Assess this cell for malaria.
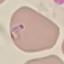
Parasitized.

stain: Giemsa
preparation: thin blood film
capture: smartphone camera at the microscope eyepiece
image_type: cell patch, automatically extracted from a larger field of view and resized to 64 × 64 pixels